Name the parasite shown.
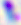

This is Toxoplasma gondii.

Summary:
  - Magnification: 400x
  - Modality: micrograph